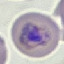 Malaria status: parasitized. Cell patch, automatically extracted from a larger field of view and resized to 64 × 64 pixels. Giemsa stain. Acquired by smartphone through the microscope eyepiece. Thin smear of blood.